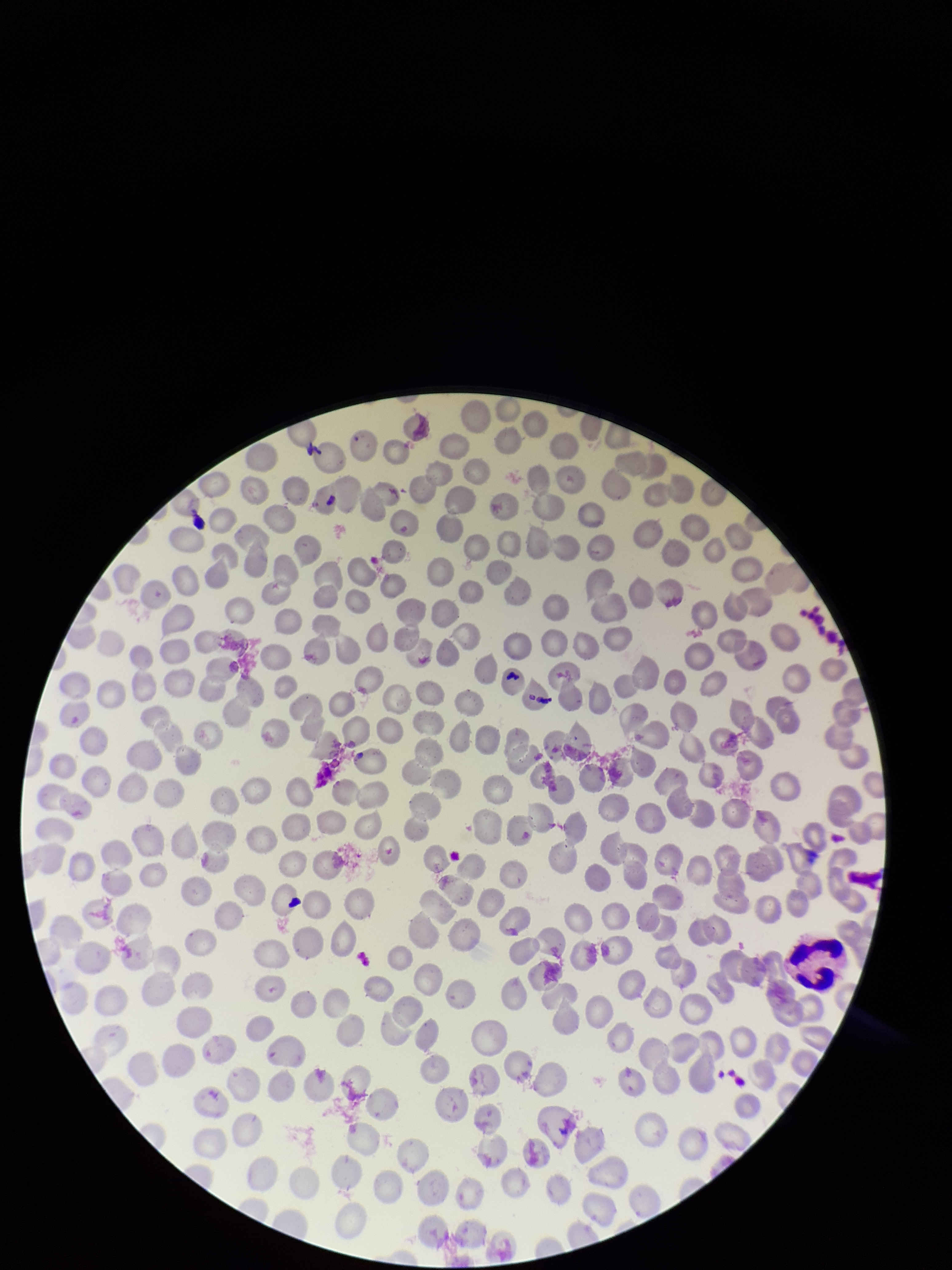

Red blood cell count: 285. One field from this slide. Photographed through the microscope eyepiece with a smartphone camera. Patient malaria status: negative. Image is 952×1270 pixels. Parasitized red blood cells: none identified. Parasitized red blood cell count: 0. Stained with Giemsa. Preparation: thin smear.